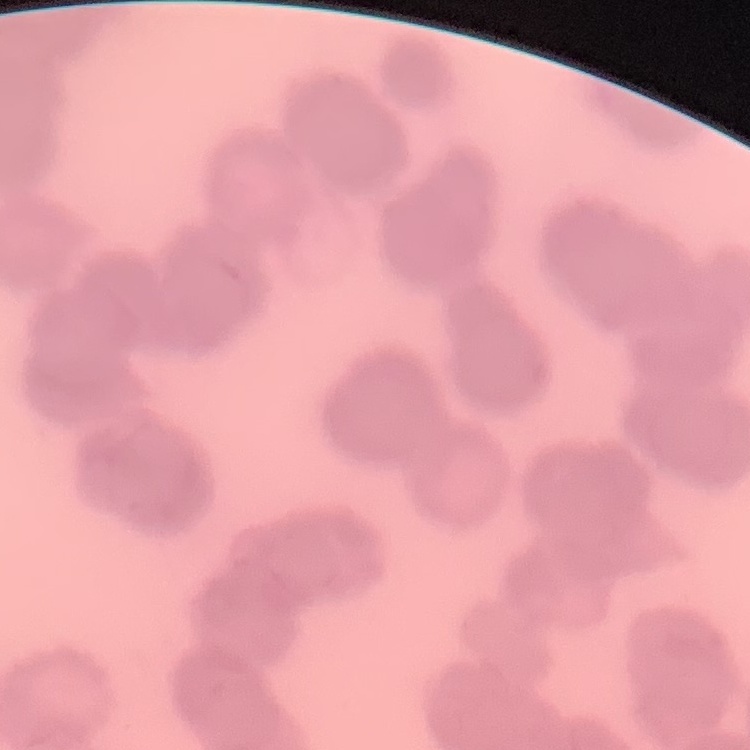
Summary:
  - Erythrocyte morphology: rouleaux formation
  - Preparation: thin blood smear
  - Image type: square crop of a larger photomicrograph
  - Stain: Field's or Giemsa